Describe the morphology of the red blood cells.
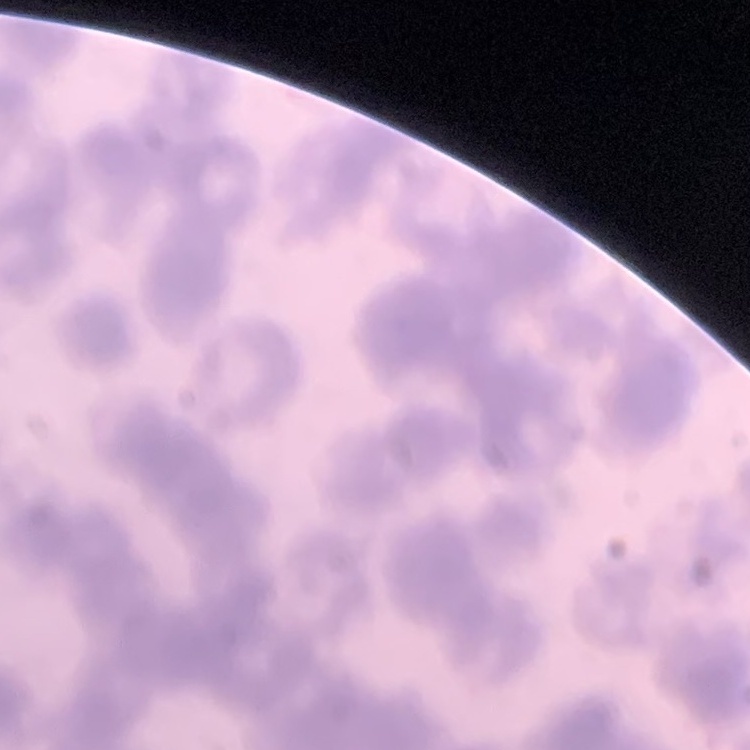

Rouleaux formation.

{
  "preparation": "thin blood smear",
  "stain": "Field's or Giemsa",
  "image_type": "square crop of a larger photomicrograph"
}